Locate every Plasmodium malariae-infected red blood cell.
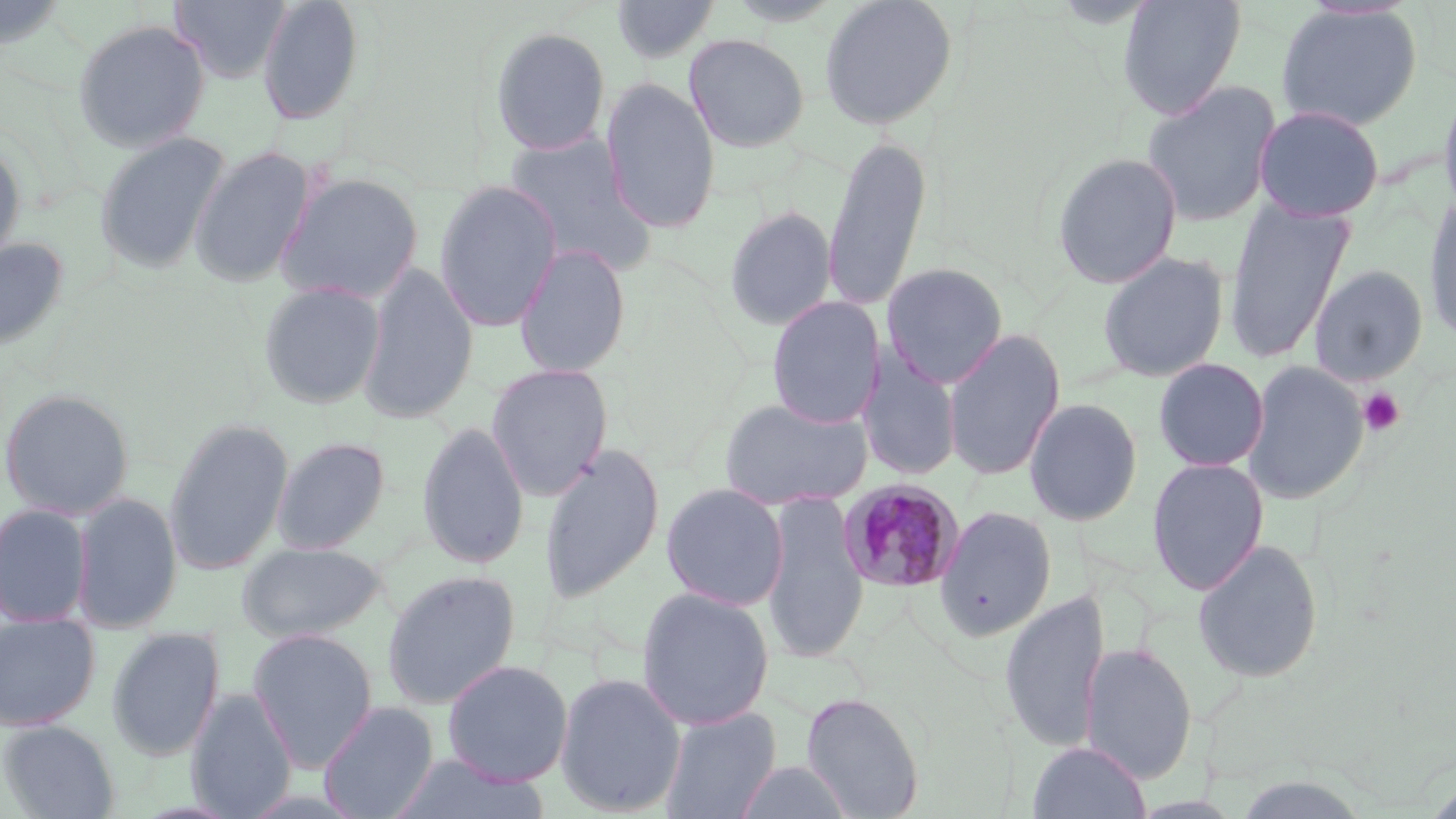

Approximate bounding boxes as [x1, y1, x2, y2] in pixels.
Plasmodium malariae-infected red blood cells: [837, 479, 965, 594].

slide_level_diagnosis: Plasmodium malariae
magnification: 1000x
image_size: 1456×819 pixels
preparation: thin blood smear
stain: May-Grünwald-Giemsa
modality: optical microscopy
uninfected_red_blood_cell_locations: 'approximate bounding boxes as [x1, y1, x2, y2] in pixels: [0, 0, 71, 52], [170, 0, 292, 83], [256, 0, 365, 126], [611, 0, 720, 64], [725, 0, 844, 26], [818, 0, 959, 131], [1118, 0, 1246, 119], [622, 1, 770, 88], [1274, 3, 1423, 131], [72, 19, 211, 152], [489, 26, 612, 157], [684, 33, 810, 153], [601, 78, 721, 233], [1438, 78, 1456, 222], [1141, 80, 1281, 227], [1253, 104, 1385, 222], [503, 131, 658, 276], [94, 132, 231, 274], [821, 134, 932, 314], [0, 140, 26, 265], [190, 145, 316, 287], [1051, 152, 1183, 290], [274, 172, 425, 305], [433, 181, 562, 331], [1422, 191, 1456, 347], [1223, 198, 1354, 364], [724, 206, 836, 331], [0, 236, 70, 352], [514, 243, 631, 379], [1097, 251, 1230, 383], [357, 262, 479, 424], [882, 262, 1009, 389], [1308, 265, 1428, 385], [257, 281, 386, 409], [766, 297, 884, 428], [942, 328, 1065, 481], [858, 348, 961, 482], [1153, 358, 1269, 472], [1242, 360, 1368, 505], [486, 363, 613, 500], [0, 388, 135, 520], [719, 396, 873, 511], [1024, 397, 1143, 526], [164, 418, 293, 575], [417, 420, 529, 571], [271, 436, 390, 554], [539, 443, 665, 606], [1147, 458, 1269, 594], [661, 483, 788, 610], [71, 492, 183, 633], [761, 492, 868, 665], [0, 503, 93, 627], [935, 506, 1057, 641], [1192, 538, 1324, 684], [236, 541, 389, 642], [381, 571, 521, 710], [636, 587, 775, 730], [998, 588, 1108, 754], [0, 613, 99, 731], [106, 628, 226, 761], [247, 628, 378, 772], [1080, 642, 1198, 783], [441, 659, 573, 786], [554, 671, 687, 816], [186, 688, 297, 819], [800, 691, 925, 819], [319, 701, 439, 819], [659, 705, 782, 819], [1, 719, 120, 818], [1028, 740, 1151, 819], [386, 754, 551, 819], [733, 759, 853, 818]'
field_of_view: single
platelet_locations: 'approximate bounding boxes as [x1, y1, x2, y2] in pixels: [1359, 387, 1405, 436]'